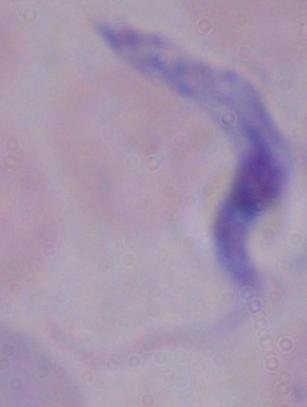
{
  "magnification": "1000x",
  "identification": "trypanosome",
  "modality": "photomicrograph"
}